Assess this cell for malaria.
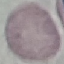

Uninfected.

Giemsa-stained preparation. Thin smear of blood. Acquired by smartphone through the microscope eyepiece. Cell patch, automatically extracted from a larger field of view and resized to 64 × 64 pixels.